Locate every malaria parasite.
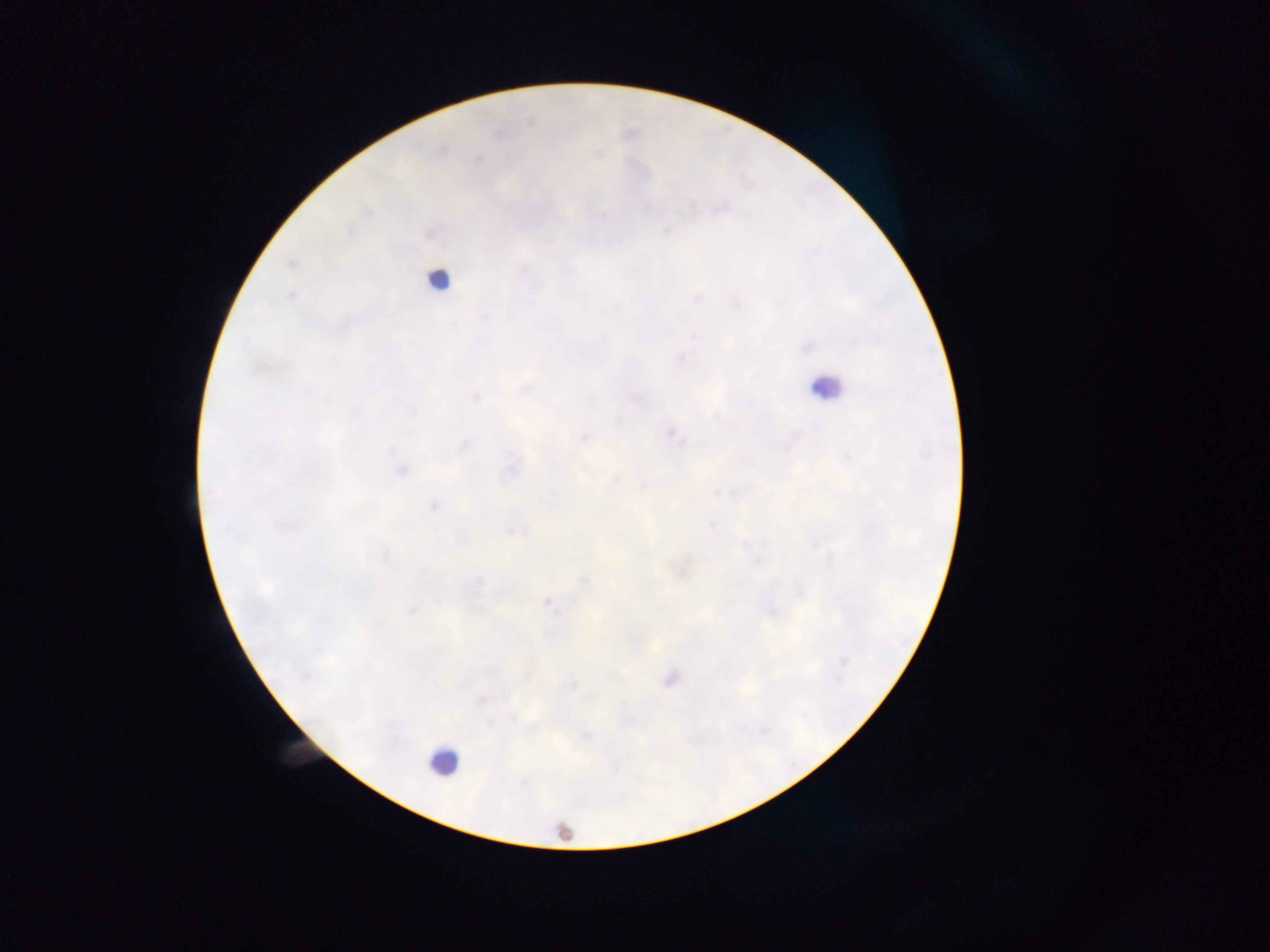
Approximate centers as x y in pixels.
Malaria parasites: 670 433; 583 437; 511 466; 400 470; 433 506; 547 600; 669 679.

{
  "leukocyte_locations": "approximate centers as x y in pixels: 439 279; 826 387; 442 762; 564 832",
  "capture": "mobile-phone photograph through a microscope",
  "image_size": "1270×952 pixels",
  "country": "Ghana",
  "field_of_view": "single",
  "preparation": "thick blood film"
}